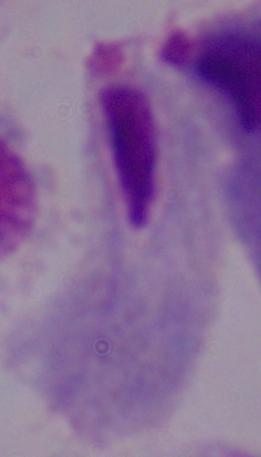 Captured at 1000x magnification. A trichomonad is shown. Micrograph.